Identify the preparation type.
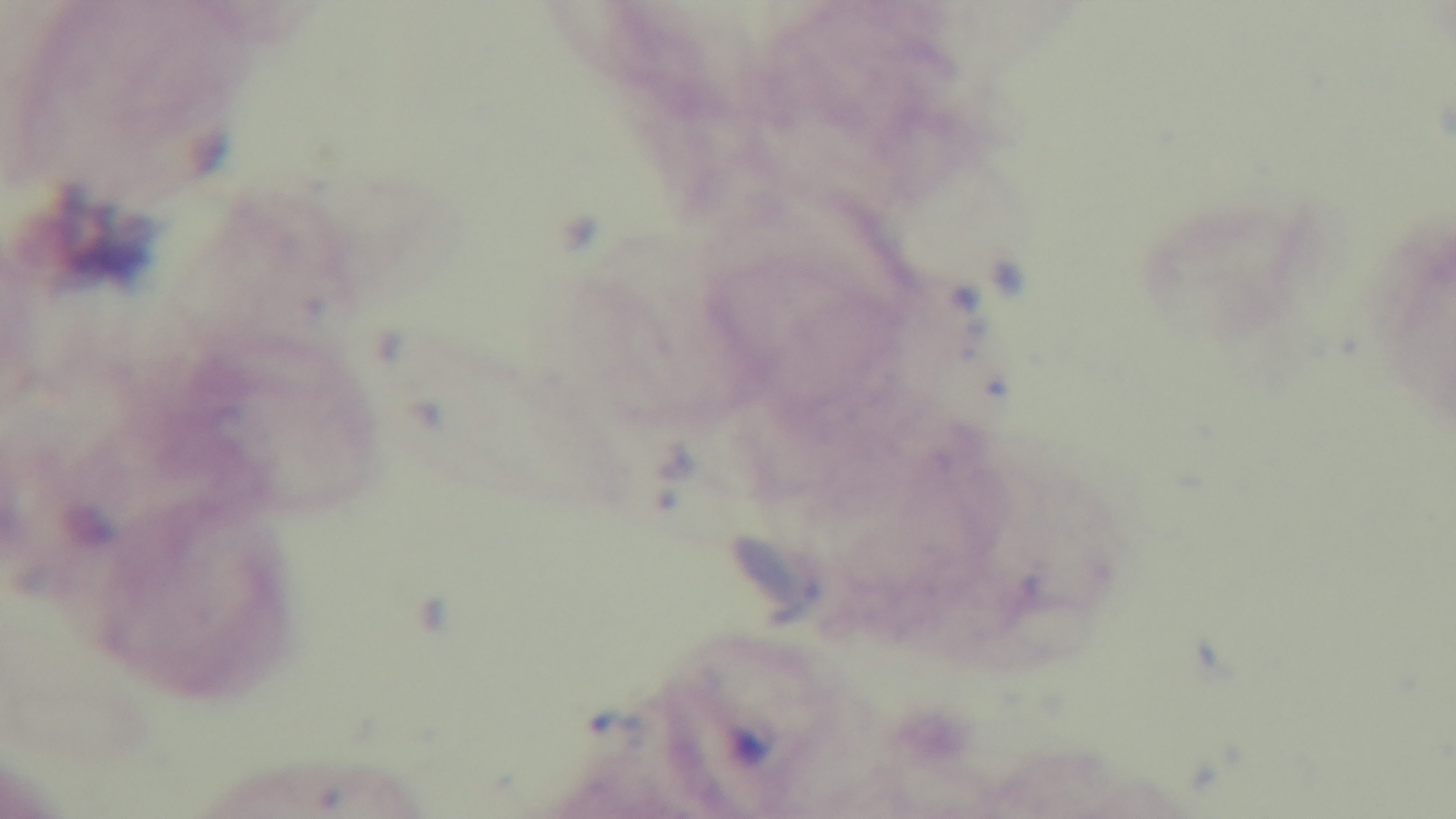

It is a thick blood film.

Summary:
  - Malaria status: negative
  - Capture: mounted 4K digital camera
  - Field of view: single
  - Modality: light microscopy
  - Stain: Giemsa
  - Objective: 100x oil immersion